Name the blood parasite species.
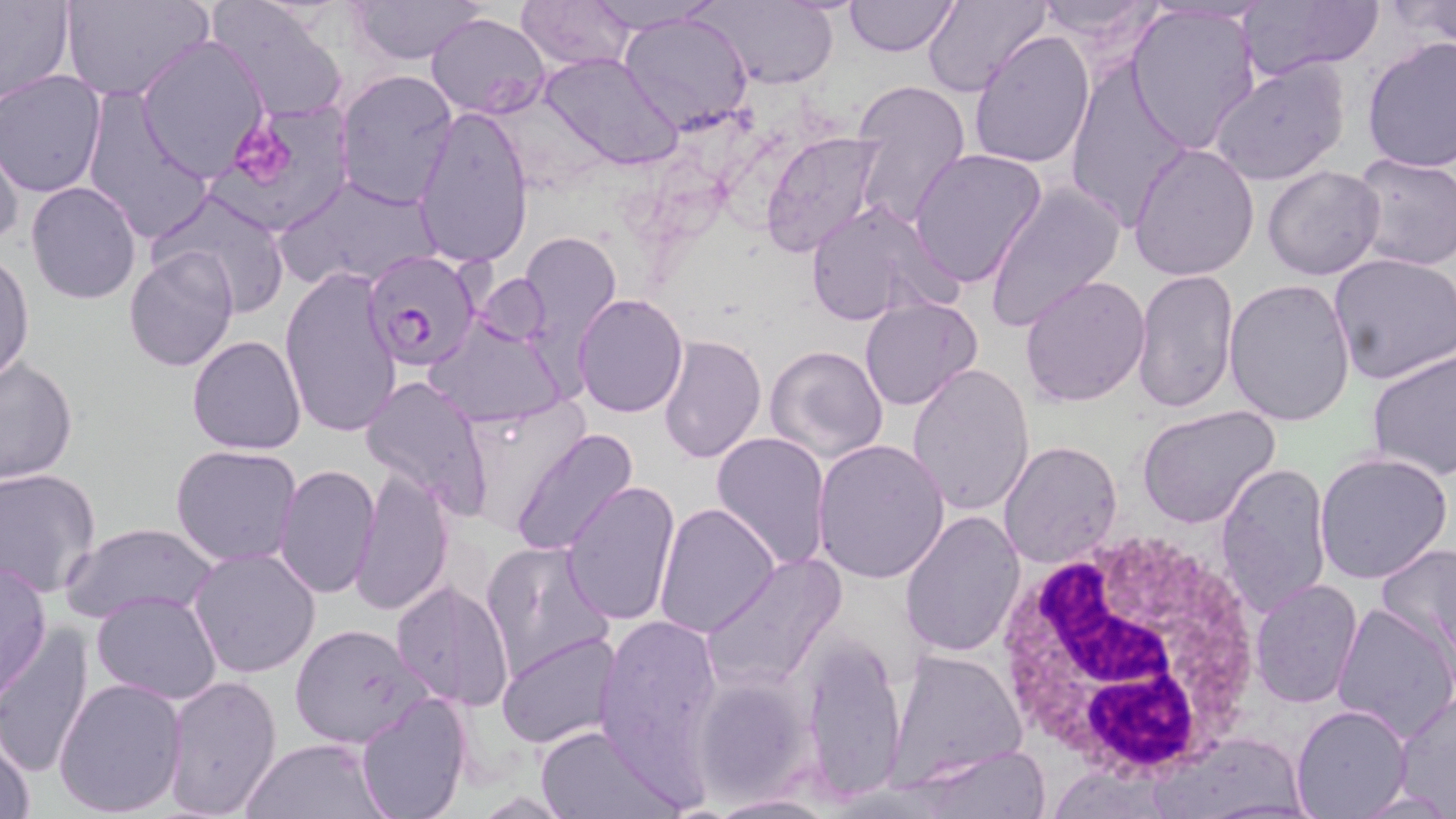
Plasmodium falciparum.

Approximate bounding boxes as [x1, y1, x2, y2] in pixels. White blood cell locations: [985, 524, 1272, 784]. Platelet locations: [237, 120, 294, 181]. Plasmodium falciparum-infected red blood cell locations: [362, 250, 481, 370]. Uninfected red blood cell locations: [62, 0, 210, 103], [205, 0, 349, 121], [351, 0, 485, 63], [843, 0, 959, 56], [920, 0, 1050, 98], [1033, 0, 1168, 55], [1232, 0, 1382, 82], [1385, 0, 1456, 50], [0, 1, 74, 106], [518, 1, 637, 71], [701, 1, 839, 88], [1124, 5, 1261, 153], [427, 12, 551, 119], [619, 12, 754, 137], [967, 30, 1095, 169], [136, 35, 270, 179], [1361, 38, 1456, 173], [538, 52, 680, 169], [1063, 55, 1195, 229], [1209, 58, 1351, 186], [335, 69, 459, 209], [0, 71, 106, 196], [849, 76, 972, 229], [81, 87, 214, 245], [211, 102, 352, 233], [413, 102, 532, 269], [760, 131, 886, 258], [0, 137, 22, 251], [1129, 144, 1260, 282], [909, 149, 1046, 290], [1349, 151, 1456, 271], [1261, 163, 1385, 280], [277, 172, 443, 292], [26, 181, 141, 303], [984, 182, 1125, 330], [151, 188, 292, 316], [804, 198, 961, 328], [517, 231, 624, 358], [123, 246, 237, 373], [1329, 251, 1456, 386], [0, 252, 34, 385], [280, 268, 402, 438], [1132, 269, 1239, 413], [1020, 276, 1151, 407], [1223, 278, 1355, 426], [573, 293, 688, 417], [860, 296, 982, 411], [426, 314, 569, 430], [658, 332, 768, 465], [188, 335, 307, 455], [764, 343, 889, 466], [1367, 349, 1456, 481], [1, 359, 77, 485], [907, 363, 1035, 517], [359, 374, 493, 516], [458, 394, 588, 532], [1137, 406, 1281, 532], [510, 429, 636, 556], [711, 432, 832, 572], [813, 437, 950, 584], [998, 440, 1123, 567], [170, 444, 302, 567], [1315, 451, 1453, 582], [1214, 460, 1333, 619], [273, 462, 379, 599], [349, 468, 454, 617], [0, 469, 102, 596], [560, 480, 682, 626], [653, 503, 779, 637], [899, 509, 1025, 657], [62, 522, 219, 624], [480, 539, 616, 683], [1377, 542, 1456, 660], [189, 546, 322, 680], [703, 554, 845, 692], [0, 559, 50, 703], [1249, 578, 1362, 707], [391, 579, 517, 711], [90, 589, 223, 707], [1331, 600, 1456, 743], [596, 614, 722, 767], [288, 623, 434, 749], [0, 628, 97, 776], [498, 633, 620, 750], [800, 633, 906, 805], [887, 648, 1028, 783], [159, 672, 283, 819], [693, 674, 815, 806], [54, 677, 187, 815], [1393, 690, 1456, 807], [355, 695, 471, 819], [1290, 704, 1412, 819], [533, 725, 682, 817], [1, 729, 37, 819], [1156, 731, 1310, 817], [240, 737, 391, 818], [904, 744, 1051, 818], [706, 792, 838, 817]. Single field of view. Thin blood smear. May-Grünwald-Giemsa stain. Captured at 1000x magnification. Light microscopy. Image is 1456×819 pixels.